Outline each blood parasite and name the species.
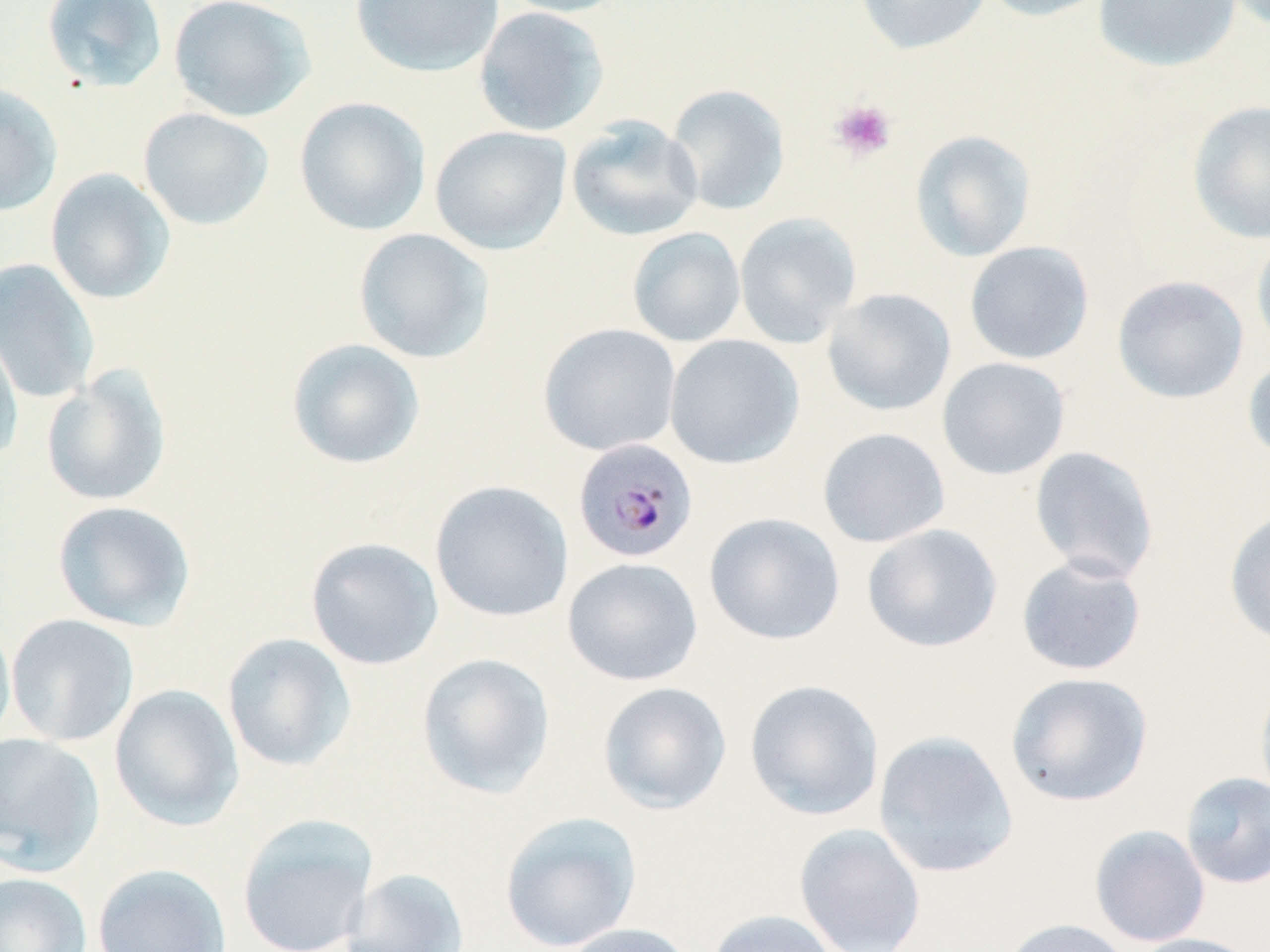

Approximate bounding boxes as (x1,y1)-(x2,y2) corner pairs in pixels.
Plasmodium malariae-infected red blood cells: (572,437)-(699,563).
No Plasmodium falciparum, Plasmodium ovale, Plasmodium vivax, Babesia divergens, or Trypanosoma brucei observed.

slide-level diagnosis = Plasmodium malariae
uninfected red blood cell locations = approximate bounding boxes as (x1,y1)-(x2,y2) corner pairs in pixels: (40,0)-(169,93), (168,0)-(315,122), (350,0)-(504,78), (493,0)-(629,18), (854,0)-(992,56), (976,0)-(1114,22), (1092,0)-(1243,74), (474,6)-(610,137), (0,82)-(63,217), (665,83)-(791,216), (294,96)-(431,236), (1187,100)-(1270,244), (137,107)-(275,231), (566,115)-(704,242), (430,125)-(572,255), (909,129)-(1037,262), (45,168)-(176,305), (733,212)-(862,348), (627,227)-(746,347), (353,228)-(495,364), (1251,232)-(1270,358), (963,241)-(1095,365), (0,258)-(100,404), (1111,275)-(1250,404), (822,288)-(957,417), (0,322)-(24,466), (538,323)-(682,456), (664,334)-(805,469), (286,338)-(425,470), (1242,354)-(1270,467), (937,357)-(1071,480), (41,365)-(173,507), (817,427)-(951,548), (1028,445)-(1161,583), (430,480)-(575,622), (51,500)-(196,631), (1224,508)-(1270,649), (703,512)-(846,646), (862,523)-(1003,653), (305,537)-(444,670), (1016,554)-(1148,676), (562,556)-(703,686), (5,614)-(140,747), (0,616)-(16,748), (222,632)-(357,772), (416,652)-(556,799), (1005,671)-(1154,808), (1255,674)-(1270,811), (744,679)-(884,821), (597,681)-(732,815), (110,684)-(244,831), (873,730)-(1019,878), (0,732)-(105,875), (1179,771)-(1270,889), (499,810)-(642,951), (236,813)-(379,952), (793,822)-(926,952), (1089,824)-(1211,947), (92,862)-(232,952), (340,867)-(471,952), (0,872)-(92,952), (704,908)-(844,952), (998,917)-(1134,952), (556,922)-(701,952), (1126,932)-(1264,952)
image size = 1270×952 pixels
platelet locations = approximate bounding boxes as (x1,y1)-(x2,y2) corner pairs in pixels: (829,99)-(897,162)
preparation = thin blood film
modality = optical microscopy
field of view = single
stain = May-Grünwald-Giemsa
magnification = 1000x